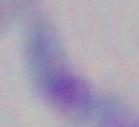

magnification = 1000x
modality = micrograph
identification = Toxoplasma gondii